Locate every uninfected red blood cell.
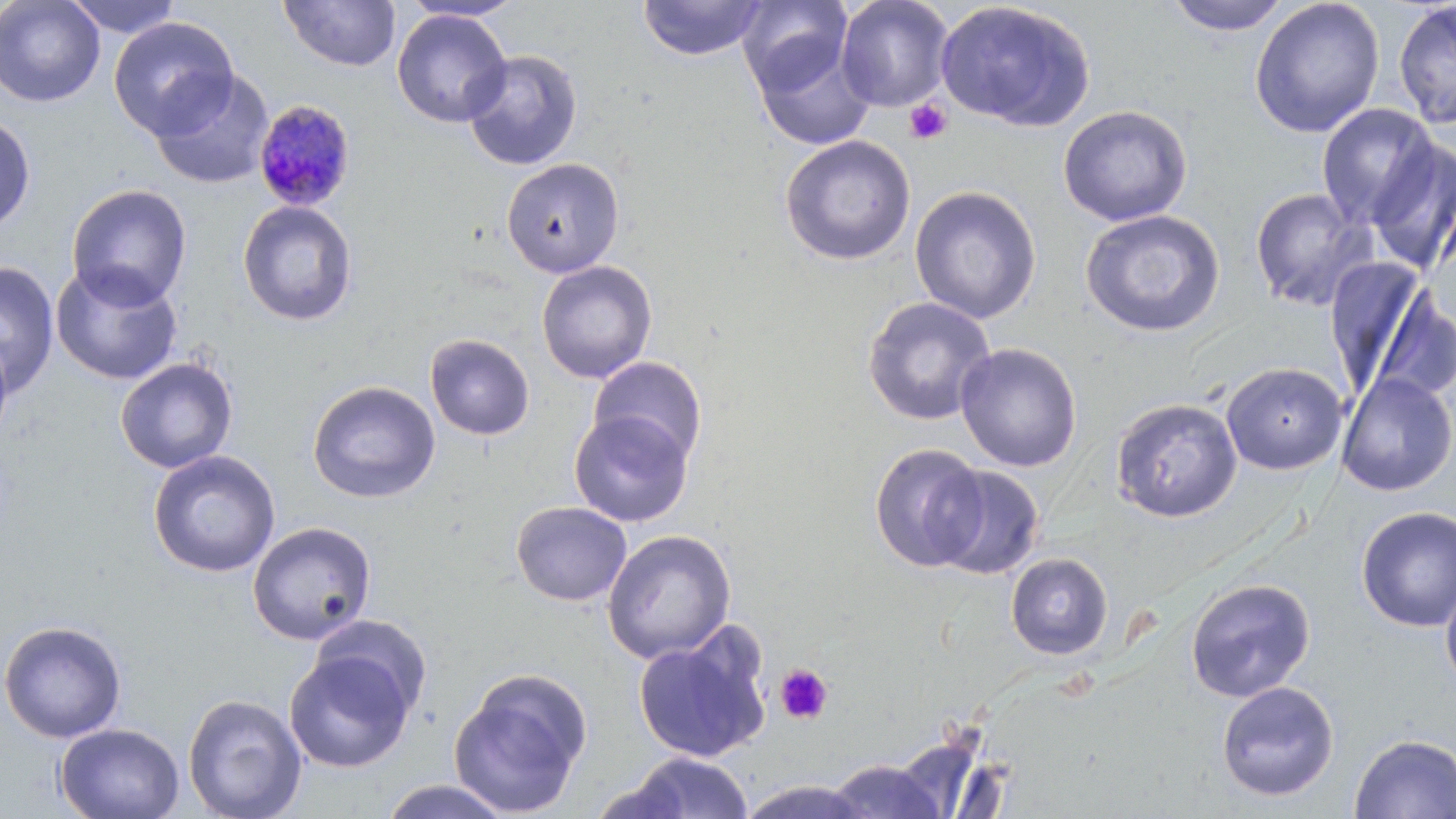

Approximate bounding boxes as [x1, y1, x2, y2] in pixels.
Uninfected red blood cells: [0, 0, 106, 108], [63, 0, 183, 38], [278, 0, 401, 73], [400, 0, 524, 21], [637, 0, 769, 62], [737, 0, 852, 96], [835, 0, 955, 113], [1164, 0, 1293, 35], [1249, 0, 1386, 138], [935, 1, 1095, 132], [1393, 2, 1456, 129], [391, 9, 512, 128], [108, 16, 239, 140], [752, 38, 877, 151], [462, 49, 583, 171], [149, 69, 274, 190], [1316, 103, 1439, 229], [1057, 105, 1193, 226], [0, 114, 36, 233], [779, 134, 916, 266], [1364, 139, 1456, 274], [501, 157, 624, 278], [66, 184, 192, 309], [909, 185, 1042, 324], [1248, 187, 1377, 312], [237, 200, 358, 326], [1080, 209, 1226, 338], [536, 260, 658, 384], [0, 262, 59, 395], [50, 262, 184, 385], [1325, 266, 1446, 404], [862, 296, 996, 426], [424, 334, 535, 441], [0, 336, 14, 447], [955, 343, 1082, 472], [589, 356, 708, 466], [115, 357, 239, 474], [1220, 361, 1348, 475], [1336, 372, 1455, 496], [307, 380, 441, 504], [1110, 398, 1243, 523], [569, 411, 693, 527], [868, 442, 989, 573], [147, 450, 281, 578], [931, 464, 1045, 580], [511, 501, 632, 606], [1355, 506, 1456, 633], [246, 521, 377, 645], [602, 529, 737, 664], [1005, 552, 1113, 660], [1184, 578, 1316, 702], [1440, 579, 1456, 691], [310, 615, 433, 720], [0, 620, 127, 743], [634, 633, 770, 764], [284, 650, 415, 773], [448, 669, 592, 817], [1215, 680, 1339, 802], [182, 693, 308, 819], [55, 723, 184, 819], [1349, 733, 1456, 818], [617, 752, 754, 818], [827, 758, 947, 818], [379, 779, 513, 818], [738, 779, 872, 818].

slide-level diagnosis = Plasmodium malariae
platelet locations = approximate bounding boxes as [x1, y1, x2, y2] in pixels: [904, 99, 953, 145], [774, 664, 833, 725]
preparation = thin blood smear
field of view = single
stain = May-Grünwald-Giemsa
image size = 1456×819 pixels
Plasmodium malariae-infected red blood cell locations = approximate bounding boxes as [x1, y1, x2, y2] in pixels: [252, 100, 356, 212]
modality = light microscopy
magnification = 1000x